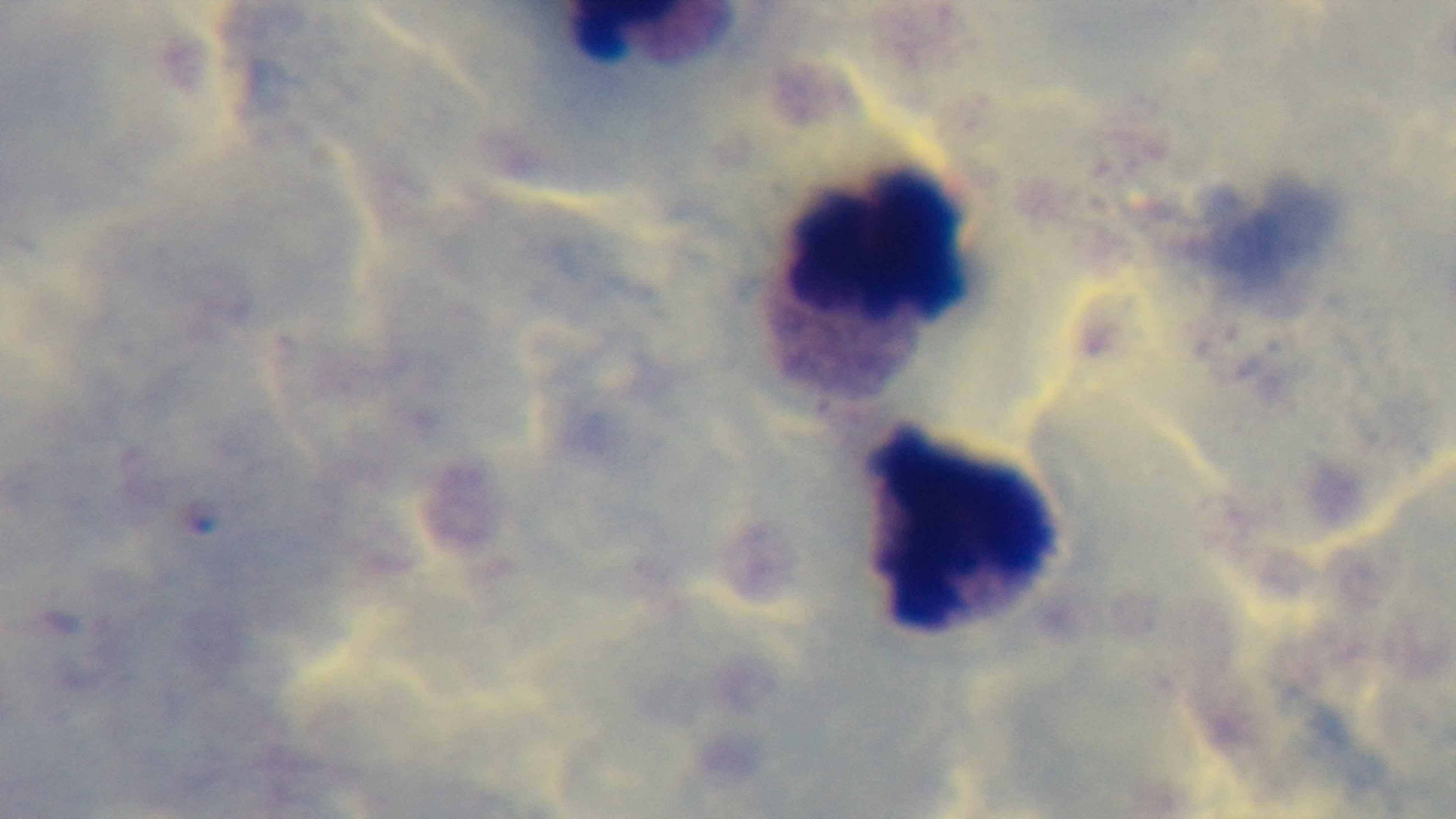
preparation = thick blood film
stain = Giemsa
modality = light microscopy
field of view = single
malaria status = negative
objective = 100x oil immersion
capture = mounted 4K digital camera